Describe the morphology of the erythrocytes.
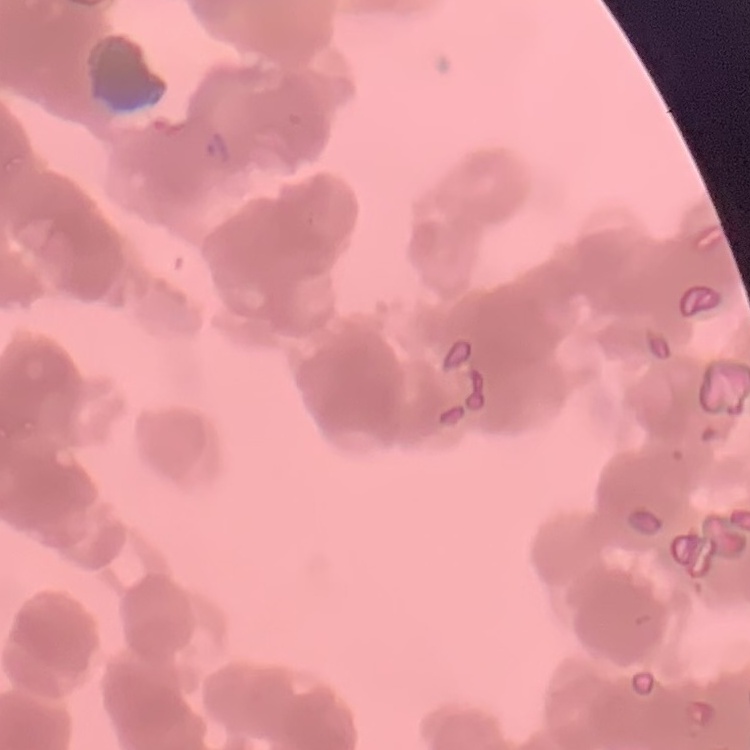

Rouleaux formation.

Square crop of a larger photomicrograph. Stained with either Field's or Giemsa. Thin peripheral smear.